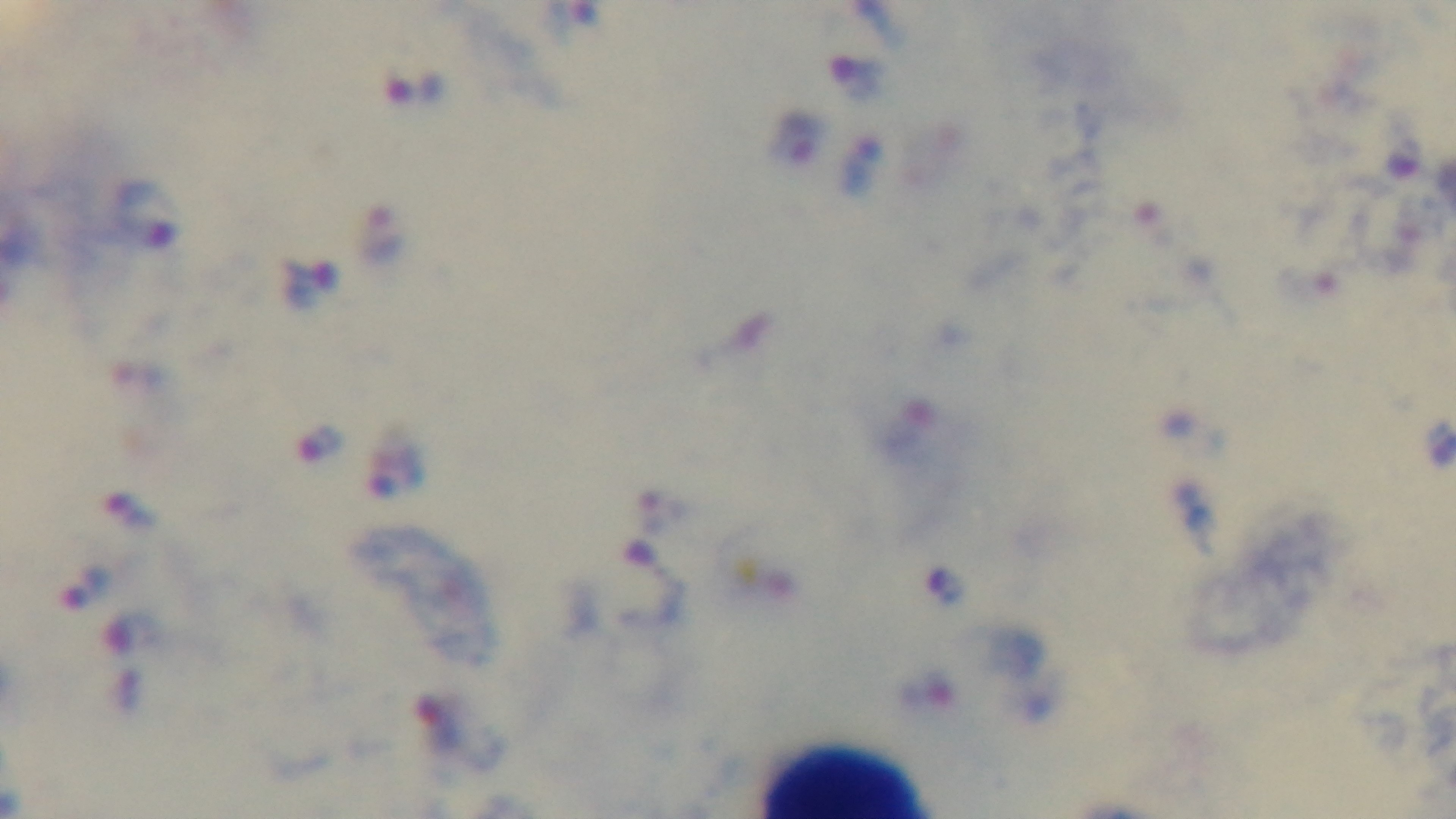
Giemsa-stained. Preparation: thick blood film. Mounted 4K digital camera. Light microscopy. Single field of view. Oil-immersion objective, 100x. Malaria status: positive.